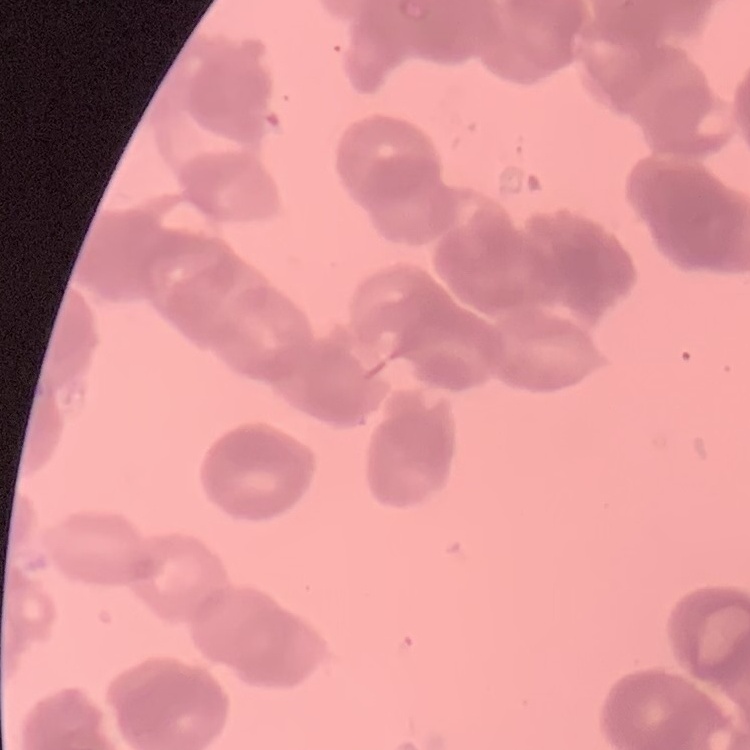
erythrocyte morphology = rouleaux formation
image type = square crop of a larger photomicrograph
preparation = thin blood film
stain = Field's or Giemsa